Outline each blood parasite and name the species.
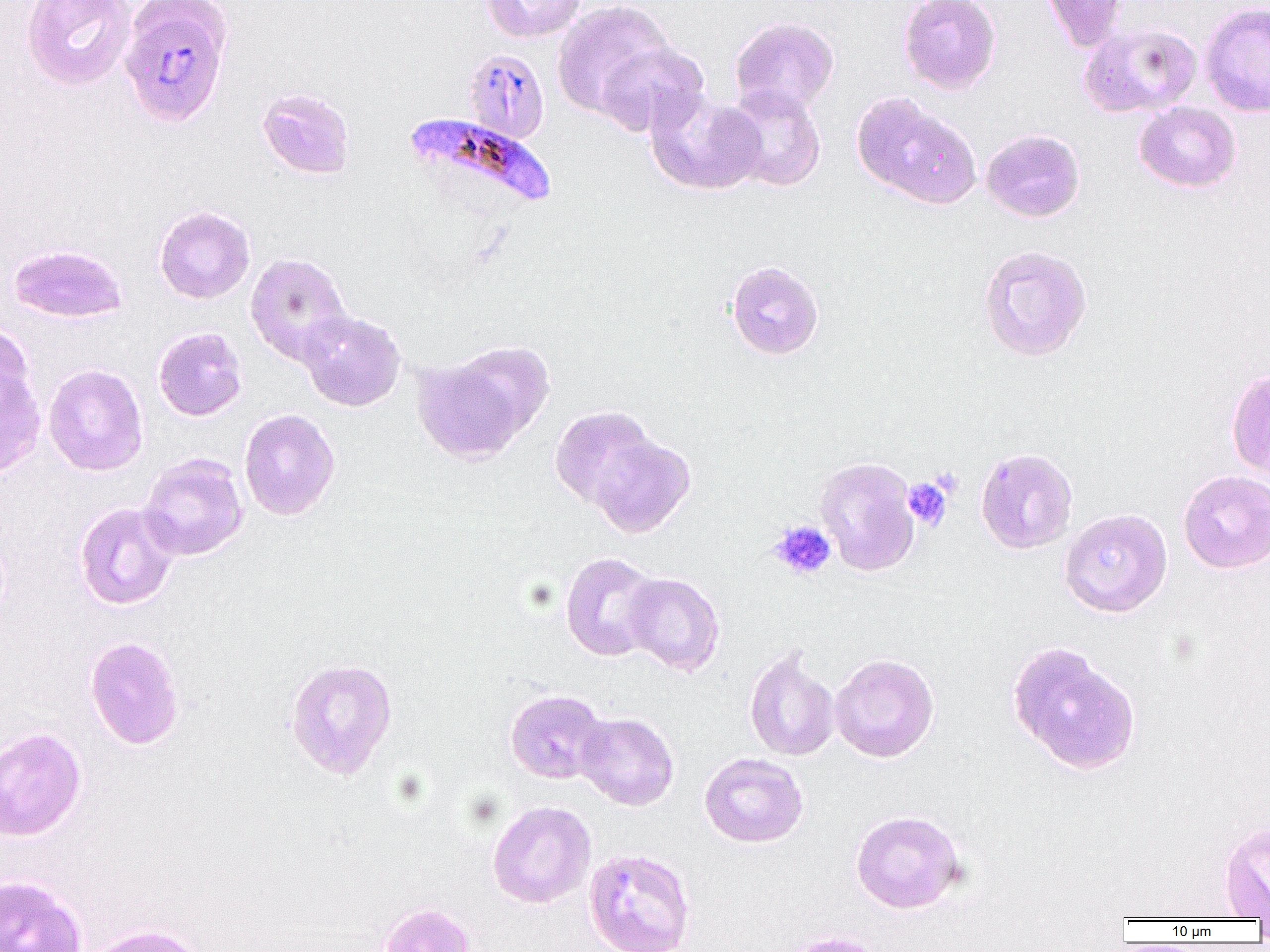

Approximate bounding boxes as (x1, y1, x2, y2) in pixels.
Plasmodium falciparum-infected red blood cells: (118, 1, 234, 128), (463, 49, 549, 144), (402, 113, 558, 216).
No Plasmodium ovale, Plasmodium malariae, Plasmodium vivax, Babesia divergens, or Trypanosoma brucei observed.

Uninfected red blood cell locations: (21, 0, 135, 91), (483, 0, 585, 42), (899, 0, 1001, 94), (1041, 0, 1128, 51), (551, 1, 675, 120), (1200, 3, 1270, 117), (730, 17, 839, 115), (1079, 22, 1202, 118), (594, 41, 709, 137), (722, 84, 827, 191), (256, 86, 356, 179), (645, 90, 765, 195), (852, 92, 981, 209), (1134, 101, 1241, 192), (981, 128, 1085, 222), (154, 205, 255, 304), (8, 244, 127, 323), (977, 244, 1093, 362), (245, 252, 353, 366), (726, 260, 824, 360), (298, 310, 406, 411), (0, 322, 36, 418), (153, 327, 247, 421), (412, 345, 546, 465), (0, 364, 46, 479), (43, 364, 148, 476), (1226, 368, 1270, 481), (550, 405, 661, 512), (239, 409, 340, 520), (586, 433, 695, 538), (975, 448, 1078, 554), (139, 453, 248, 561), (815, 456, 920, 576), (1178, 470, 1270, 573), (74, 501, 180, 611), (1059, 508, 1172, 617), (560, 551, 661, 661), (622, 572, 725, 675), (84, 636, 184, 750), (1007, 641, 1141, 776), (744, 647, 840, 761), (829, 653, 940, 763), (284, 657, 398, 780), (504, 689, 607, 784), (575, 712, 679, 810), (0, 727, 86, 841), (699, 752, 808, 848), (487, 800, 596, 908), (850, 810, 965, 913), (1219, 822, 1270, 919), (584, 847, 696, 952), (0, 875, 88, 952), (378, 902, 477, 952), (82, 924, 211, 952), (779, 931, 888, 952). Platelet locations: (931, 467, 962, 498), (902, 477, 952, 530), (769, 520, 837, 580). Slide-level diagnosis: Plasmodium falciparum. One field of a larger specimen. Image is 1270×952 pixels. Captured at 1000x magnification. Optical microscopy. Thin blood smear.